Locate every blood parasite and identify its species.
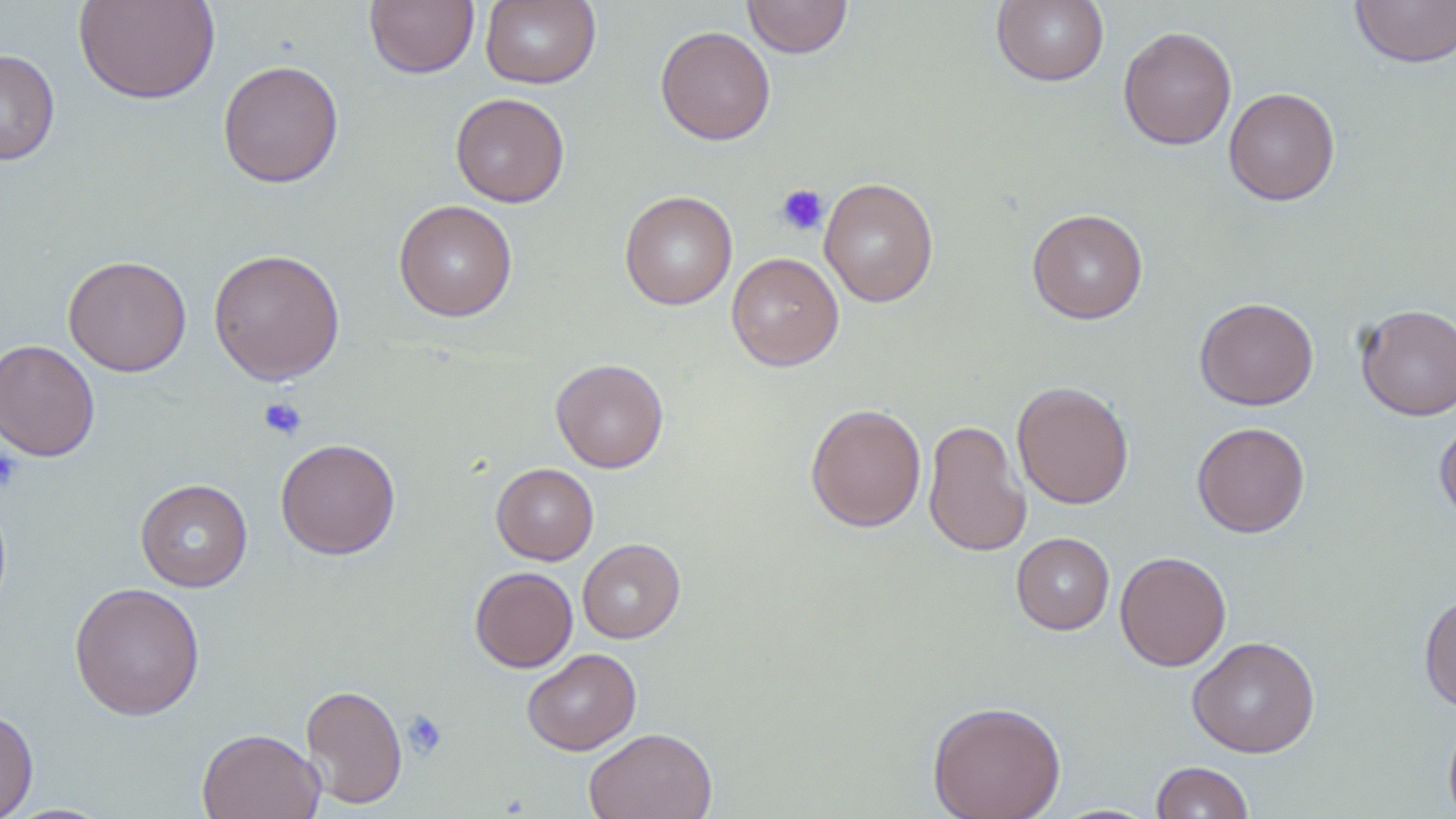
No blood parasites seen.

{
  "slide_level_diagnosis": "no evidence of blood parasites",
  "modality": "light microscopy",
  "uninfected_red_blood_cell_locations": "approximate bounding boxes as (x1, y1, x2, y2) in pixels: (73, 0, 220, 105), (480, 0, 601, 89), (742, 0, 853, 58), (991, 0, 1110, 86), (1350, 0, 1455, 68), (364, 1, 480, 78), (655, 26, 775, 145), (1117, 26, 1236, 150), (0, 49, 59, 165), (217, 60, 344, 187), (1223, 86, 1341, 206), (450, 92, 569, 207), (819, 177, 938, 307), (620, 190, 737, 310), (393, 200, 518, 322), (1027, 209, 1148, 324), (208, 248, 345, 385), (726, 252, 844, 371), (63, 255, 192, 377), (1194, 297, 1319, 410), (1355, 303, 1455, 420), (0, 338, 101, 462), (551, 358, 668, 473), (1012, 380, 1134, 510), (805, 403, 927, 532), (1434, 417, 1456, 528), (922, 419, 1031, 556), (1193, 422, 1311, 538), (275, 438, 401, 560), (491, 463, 599, 565), (136, 479, 252, 591), (1011, 532, 1115, 635), (578, 539, 685, 643), (1114, 550, 1231, 671), (470, 566, 577, 672), (69, 582, 205, 721), (1419, 593, 1456, 712), (1187, 636, 1320, 758), (522, 648, 641, 755), (300, 683, 408, 809), (926, 700, 1066, 819), (0, 709, 39, 819), (1443, 712, 1456, 819), (583, 727, 718, 819), (197, 728, 325, 819), (1150, 761, 1254, 819)",
  "magnification": "1000x",
  "field_of_view": "single",
  "stain": "May-Grünwald-Giemsa",
  "image_size": "1456×819 pixels",
  "platelet_locations": "approximate bounding boxes as (x1, y1, x2, y2) in pixels: (775, 184, 829, 237), (258, 397, 307, 441), (0, 447, 24, 492), (402, 710, 447, 760)",
  "preparation": "thin blood smear"
}